Identify the cell.
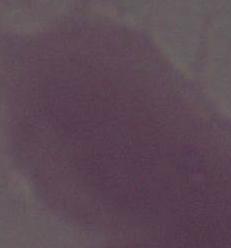
This is an erythrocyte.

Captured at 1000x magnification. Photomicrograph.